Name the cell type shown.
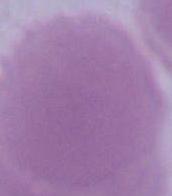

An erythrocyte.

Summary:
  - Magnification: 1000x
  - Modality: photomicrograph